Assess this cell for malaria.
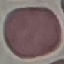
It is uninfected.

Photographed with a smartphone camera at the microscope eyepiece. Automatically extracted cell patch, resized to 64 × 64 pixels. Thin smear of blood. Giemsa-stained preparation.